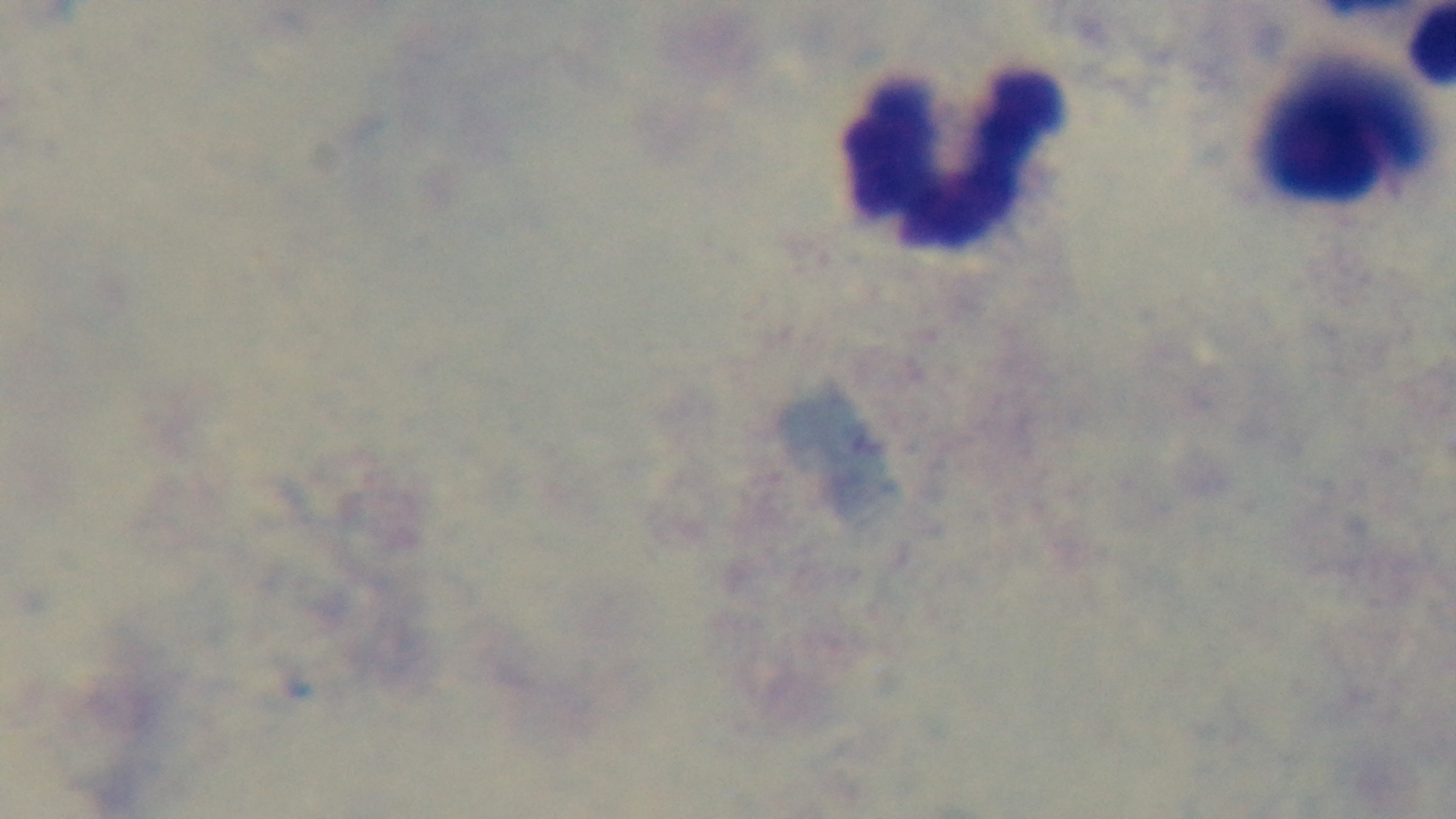
{
  "malaria_status": "uninfected",
  "field_of_view": "single",
  "modality": "light microscopy",
  "capture": "mounted 4K digital camera",
  "objective": "100x oil immersion",
  "stain": "Giemsa",
  "preparation": "thick smear"
}